Identify the cell.
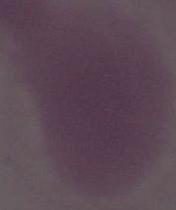

This is an erythrocyte.

Summary:
  - Modality: photomicrograph
  - Magnification: 1000x